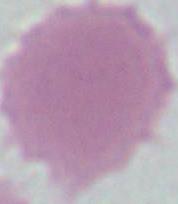

{
  "modality": "micrograph",
  "identification": "red blood cell",
  "magnification": "1000x"
}